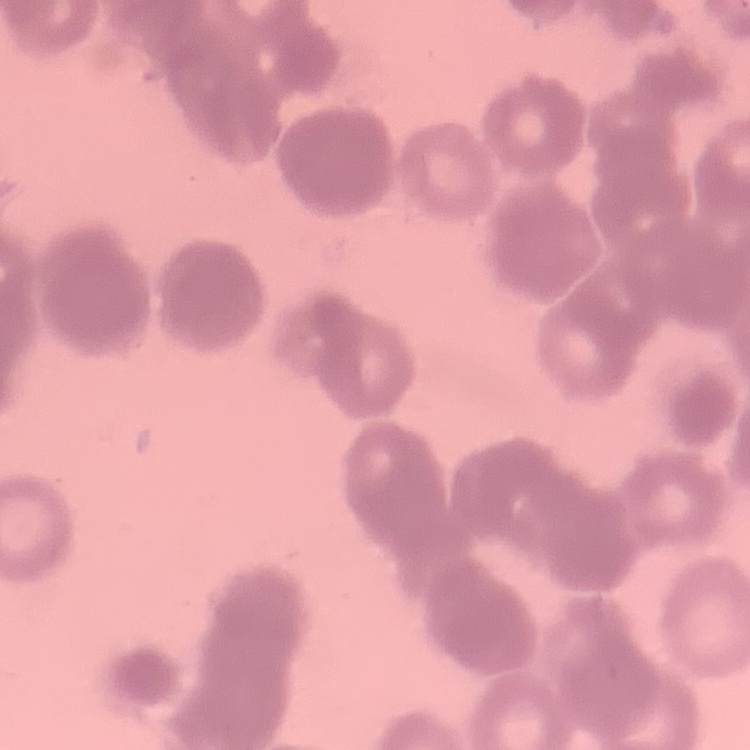
Summary:
  - Red blood cell morphology: rouleaux formation
  - Image type: square crop of a larger photomicrograph
  - Stain: Field's or Giemsa
  - Preparation: thin blood film